Classify this cell by malaria status.
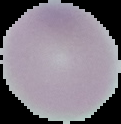

It is uninfected.

Summary:
  - Image size: 121×124 pixels
  - Preparation: thin blood film
  - Image type: segmented cell region on a black background